Classify this cell by malaria status.
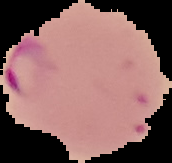

It is parasitized.

image size = 172×163 pixels
image type = segmented cell region on a black background
preparation = thin blood smear